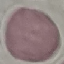
Summary:
  - Malaria status: uninfected
  - Capture: smartphone camera at the microscope eyepiece
  - Preparation: thin blood smear
  - Stain: Giemsa
  - Image type: automatically extracted cell patch, resized to 64 × 64 pixels